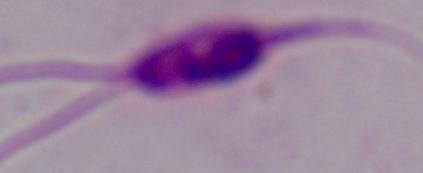

modality = photomicrograph
magnification = 1000x
identification = Leishmania